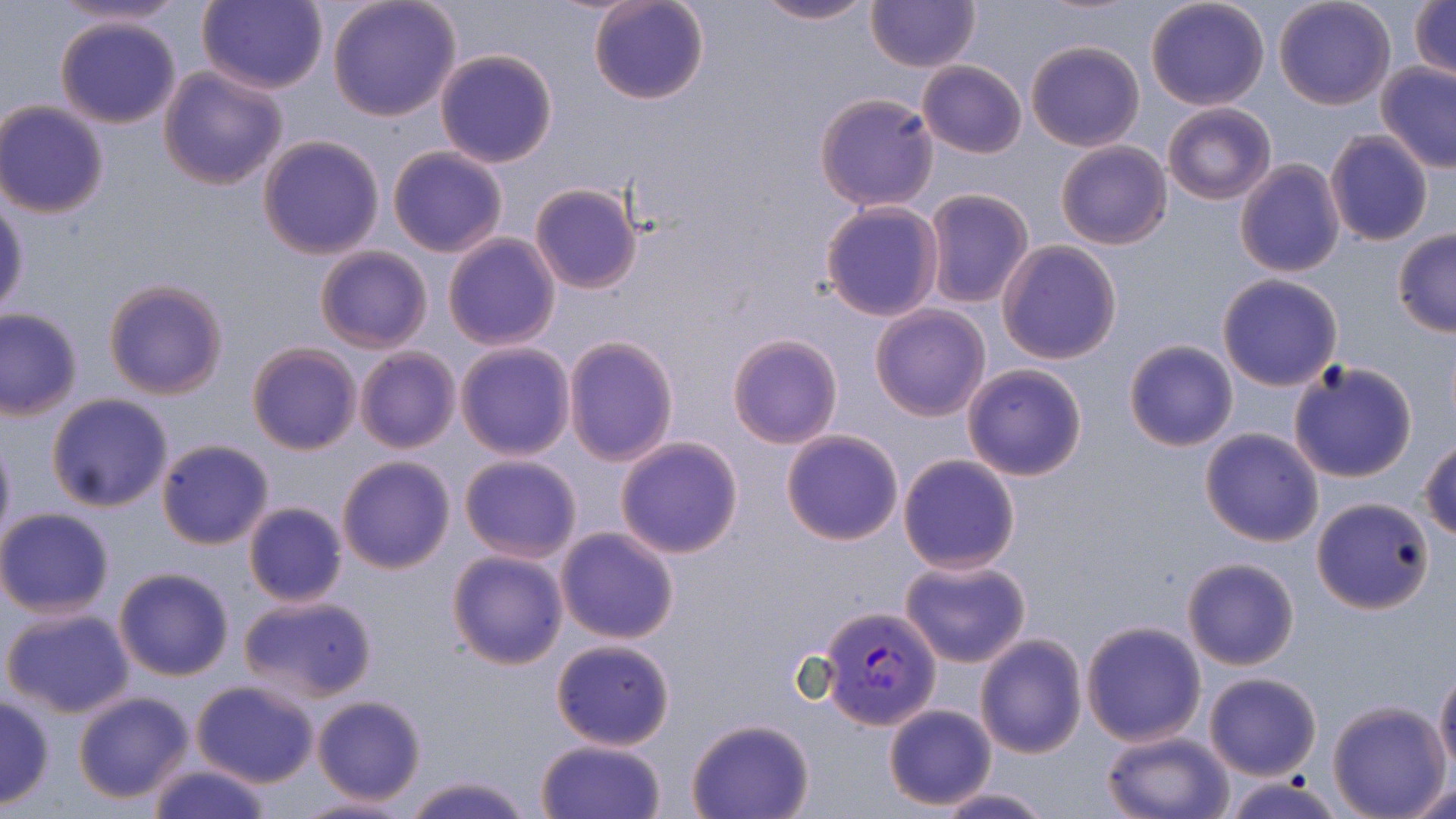
Summary:
  - Coordinate format: approximate bounding boxes as (x1, y1, x2, y2) in pixels
  - Uninfected red blood cell locations: (50, 0, 189, 29), (327, 0, 462, 121), (750, 0, 878, 25), (1145, 0, 1270, 111), (1273, 0, 1395, 109), (1410, 0, 1456, 83), (198, 1, 329, 94), (588, 1, 709, 106), (867, 2, 980, 72), (55, 15, 182, 129), (1026, 39, 1145, 151), (434, 49, 559, 167), (917, 60, 1026, 158), (1377, 62, 1456, 174), (158, 64, 288, 190), (815, 92, 939, 211), (0, 100, 109, 219), (1163, 104, 1276, 204), (1325, 130, 1434, 247), (257, 134, 386, 259), (1055, 140, 1171, 249), (387, 146, 508, 258), (1234, 158, 1345, 278), (530, 183, 642, 295), (922, 188, 1035, 310), (0, 197, 30, 316), (820, 201, 944, 321), (1391, 229, 1456, 338), (442, 233, 560, 351), (997, 241, 1124, 366), (315, 245, 433, 354), (1216, 273, 1344, 392), (103, 278, 228, 400), (870, 305, 993, 422), (0, 308, 85, 419), (564, 334, 677, 466), (727, 334, 843, 449), (1123, 339, 1238, 452), (248, 341, 360, 455), (455, 342, 576, 460), (355, 348, 461, 454), (1287, 359, 1419, 483), (962, 363, 1088, 481), (47, 394, 174, 512), (1200, 427, 1325, 547), (782, 429, 905, 546), (0, 433, 16, 549), (615, 437, 743, 558), (155, 438, 275, 550), (1419, 439, 1456, 541), (780, 444, 1021, 562), (458, 453, 583, 563), (897, 454, 1020, 573), (336, 455, 455, 575), (1312, 494, 1434, 612), (243, 502, 348, 607), (0, 508, 116, 617), (554, 527, 680, 645), (446, 550, 569, 671), (900, 556, 1032, 669), (1182, 557, 1298, 670), (114, 567, 234, 681), (240, 595, 377, 703), (2, 603, 136, 720), (1081, 621, 1206, 746), (975, 634, 1087, 759), (550, 637, 676, 751), (1435, 669, 1456, 774), (1204, 671, 1321, 780), (192, 679, 320, 787), (72, 691, 196, 805), (313, 695, 426, 806), (0, 696, 54, 808), (1327, 701, 1452, 818), (883, 704, 996, 811), (685, 718, 815, 819), (1100, 729, 1234, 819), (537, 740, 668, 819), (143, 762, 273, 819), (402, 772, 531, 819), (1397, 776, 1456, 818), (1222, 777, 1346, 818), (927, 785, 1057, 818), (288, 794, 419, 818)
  - Plasmodium vivax-infected red blood cell locations: (821, 604, 941, 728)
  - Slide-level diagnosis: Plasmodium vivax
  - Magnification: 1000x
  - Field of view: single
  - Stain: May-Grünwald-Giemsa
  - Preparation: thin blood film
  - Modality: optical microscopy
  - Image size: 1456×819 pixels